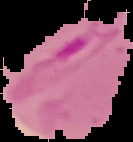

image_size: 133×142 pixels
preparation: thin blood film
malaria_status: parasitized
image_type: segmented cell region with the area outside set to black